Evaluate for Plasmodium parasites.
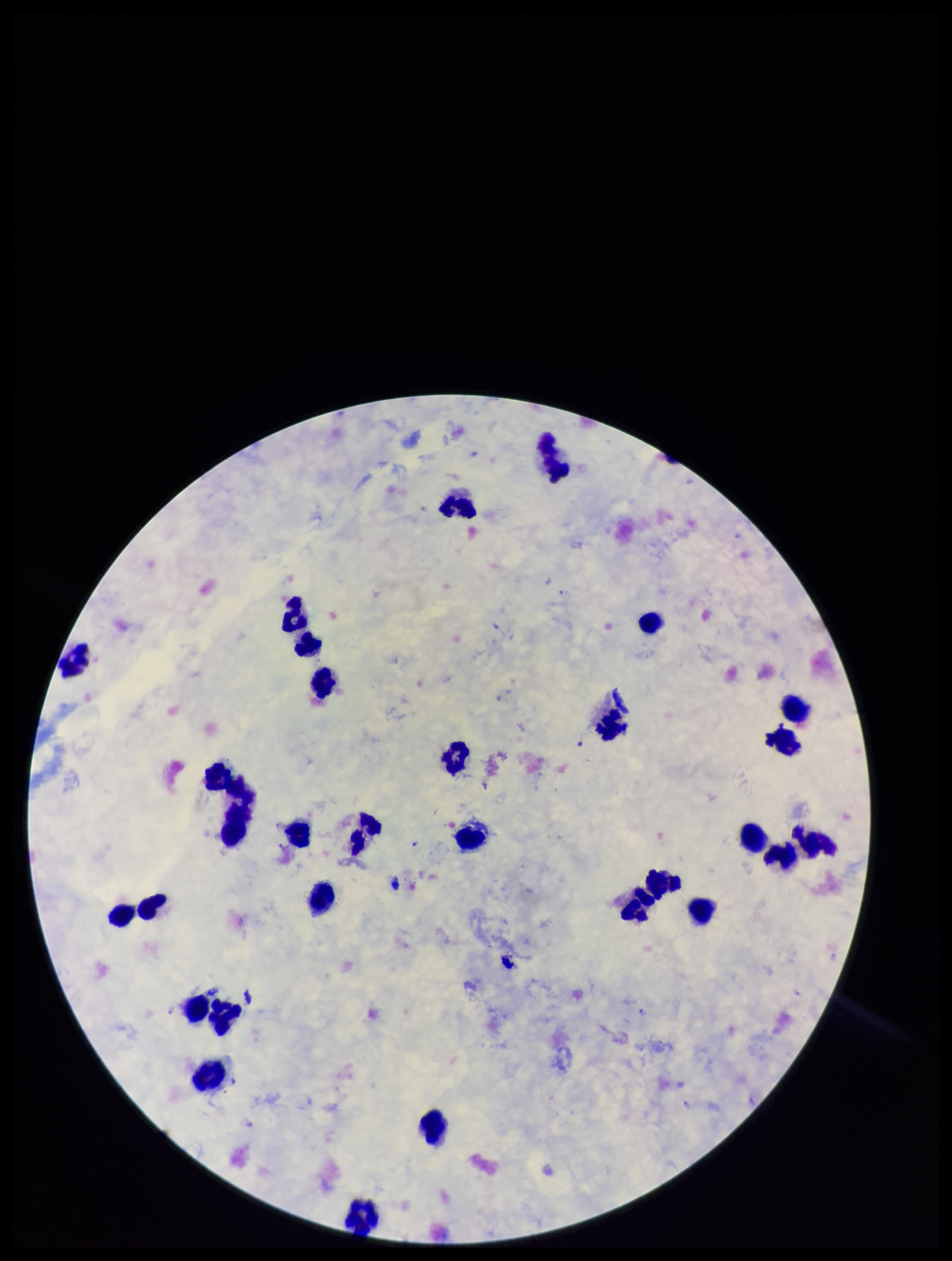

Identified.

One field from this slide. Leukocyte count: 31. Parasite count: 5. Patient malaria status: positive. Species reported for this patient: Plasmodium falciparum. Image is 952×1261 pixels. Photographed through the microscope eyepiece with a smartphone camera. Stained with Giemsa. Preparation: thick.